Describe the morphology of the erythrocytes.
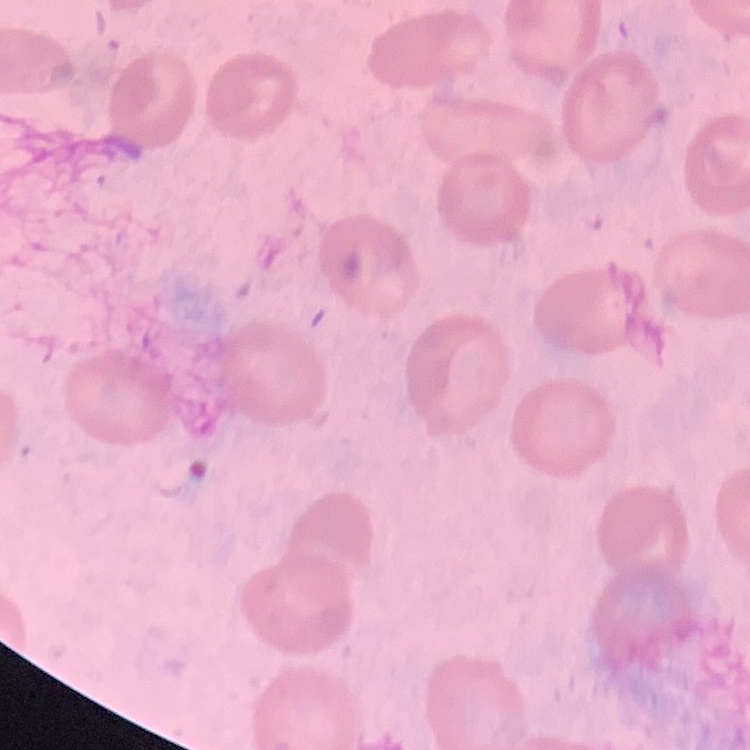

They show no rouleaux formation.

Summary:
  - Preparation: thin blood film
  - Stain: Field's or Giemsa
  - Image type: square crop of a larger photomicrograph